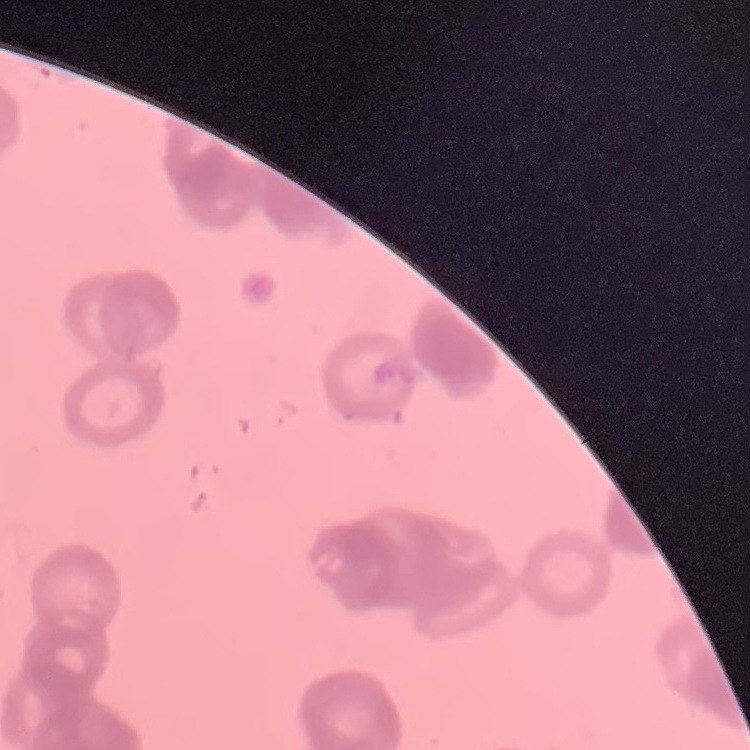

Summary:
  - Red blood cell morphology: rouleaux formation
  - Image type: one tile cut from a larger photomicrograph
  - Stain: Field's or Giemsa
  - Preparation: thin blood film